Give the preparation type.
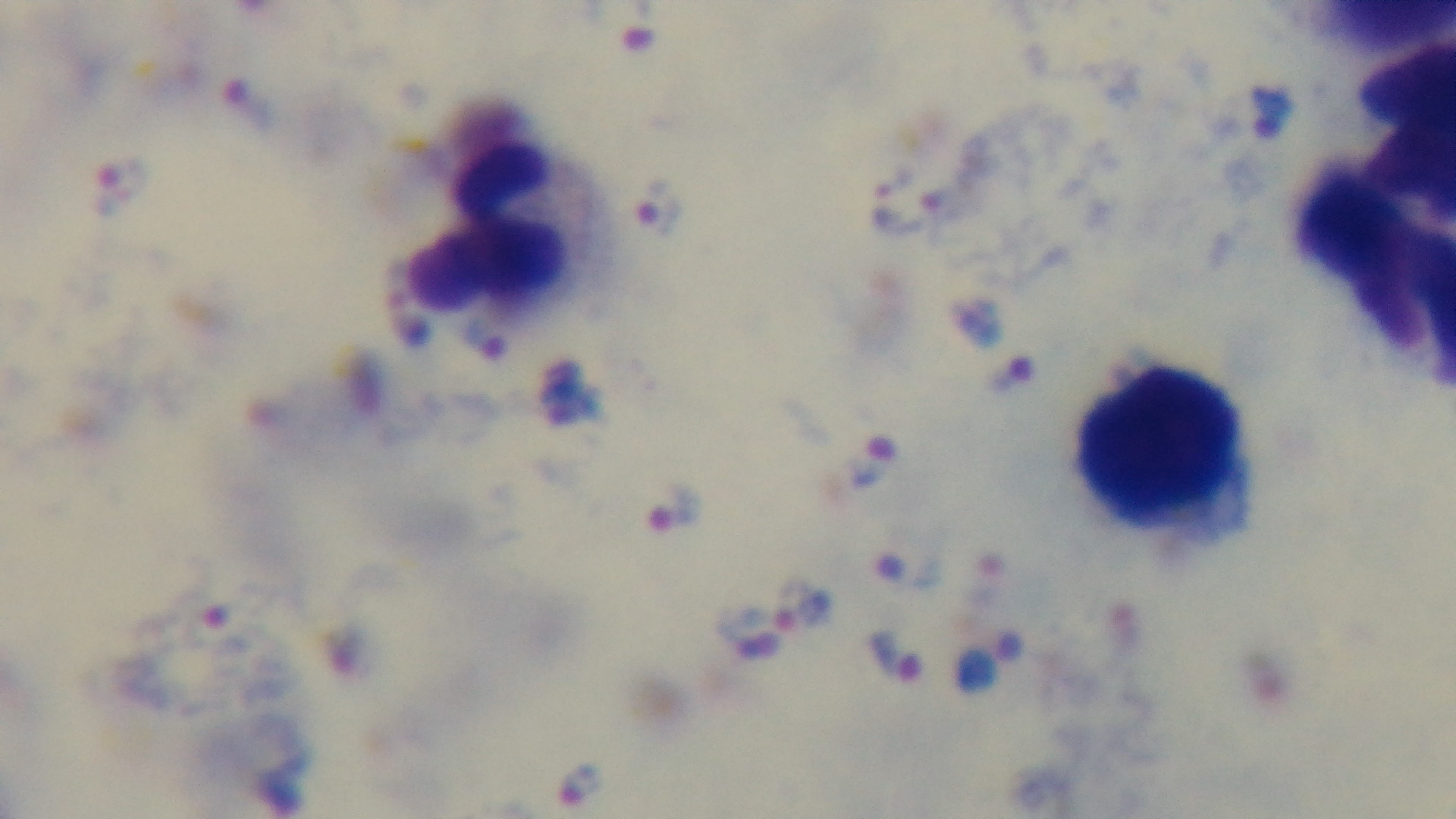

Thick.

Summary:
  - Malaria status: infected
  - Objective: 100x oil immersion
  - Stain: Giemsa
  - Modality: light microscopy
  - Field of view: single
  - Capture: mounted 4K digital camera